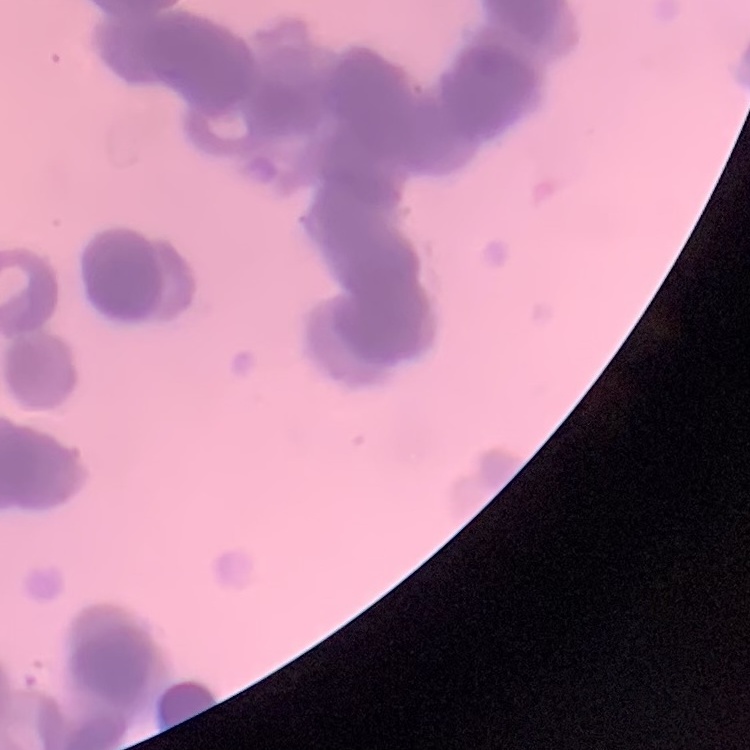

Summary:
  - Red blood cell morphology: rouleaux formation
  - Preparation: thin blood smear
  - Stain: Field's or Giemsa
  - Image type: square crop of a larger photomicrograph